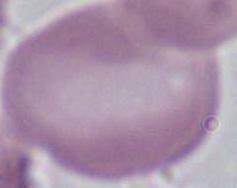
modality: photomicrograph
identification: red blood cell
magnification: 1000x